State which cell type is depicted.
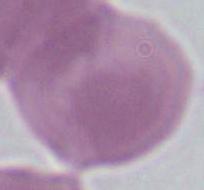

This is an erythrocyte.

Summary:
  - Modality: photomicrograph
  - Magnification: 1000x